Locate every Plasmodium falciparum-infected red blood cell.
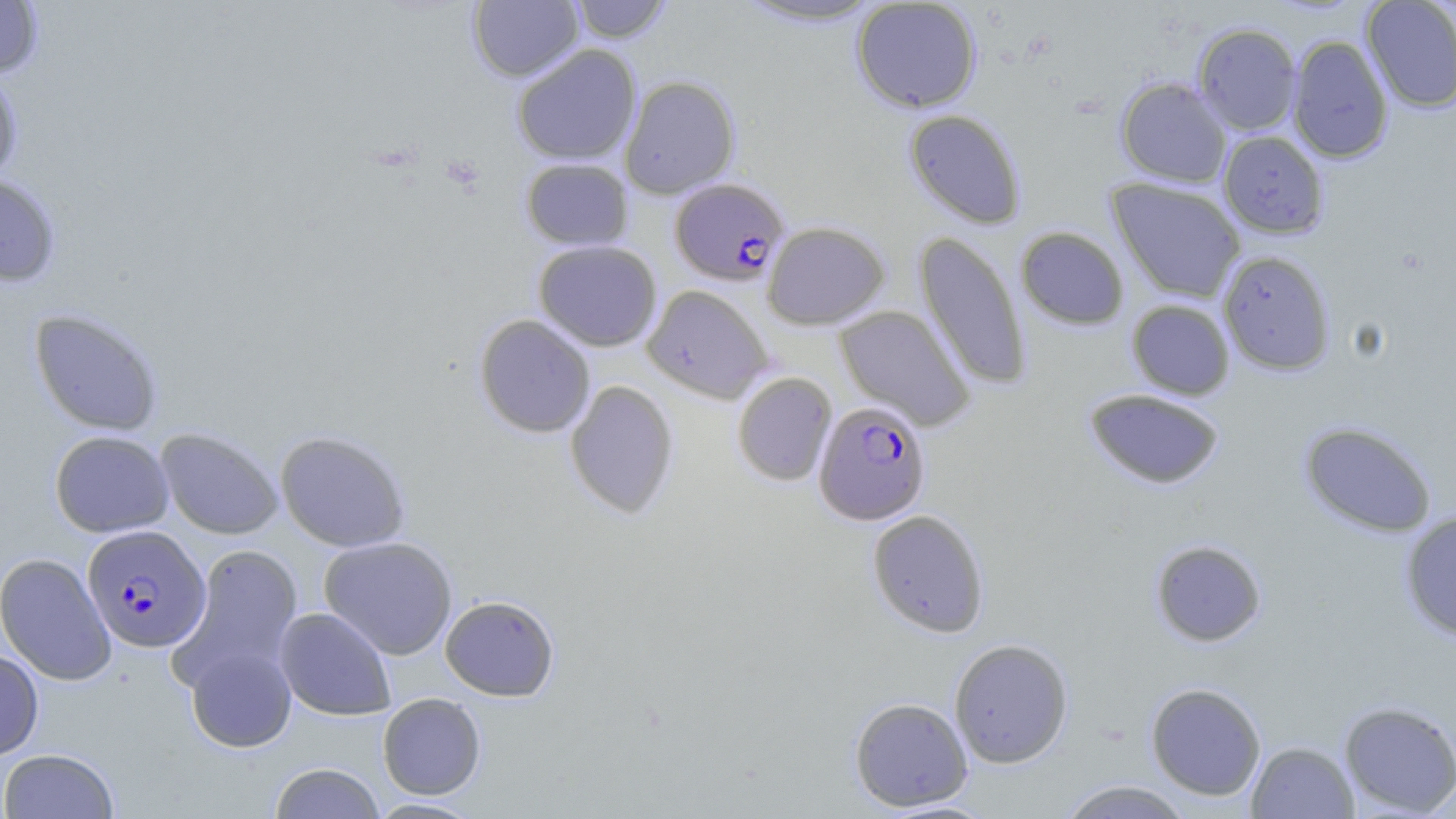
Approximate bounding boxes as (x1, y1, x2, y2) in pixels.
Plasmodium falciparum-infected red blood cells: (670, 178, 790, 286), (813, 400, 931, 525), (82, 525, 211, 653).

{
  "slide_level_diagnosis": "Plasmodium falciparum",
  "stain": "May-Grünwald-Giemsa",
  "image_size": "1456×819 pixels",
  "field_of_view": "single",
  "magnification": "1000x",
  "uninfected_red_blood_cell_locations": "approximate bounding boxes as (x1, y1, x2, y2) in pixels: (468, 0, 583, 82), (567, 0, 673, 43), (851, 0, 982, 113), (1361, 0, 1456, 113), (0, 1, 44, 79), (732, 1, 887, 28), (1193, 23, 1302, 135), (1287, 35, 1394, 163), (512, 44, 641, 165), (0, 67, 24, 186), (620, 75, 741, 199), (1116, 76, 1232, 188), (904, 109, 1027, 229), (1218, 131, 1329, 239), (520, 158, 634, 251), (0, 172, 61, 288), (1107, 178, 1246, 303), (762, 221, 889, 329), (1016, 226, 1129, 330), (914, 231, 1031, 391), (533, 240, 662, 351), (1218, 251, 1336, 376), (642, 285, 774, 404), (1127, 299, 1235, 400), (835, 305, 975, 431), (29, 308, 164, 435), (474, 314, 596, 438), (732, 372, 837, 487), (564, 380, 679, 519), (1083, 389, 1226, 490), (1299, 421, 1438, 538), (156, 427, 283, 540), (49, 430, 174, 537), (275, 430, 411, 552), (867, 509, 990, 637), (1399, 510, 1456, 641), (319, 536, 457, 660), (1149, 539, 1267, 647), (171, 544, 304, 690), (0, 552, 116, 686), (440, 595, 560, 701), (274, 607, 397, 720), (949, 638, 1074, 768), (185, 644, 297, 752), (0, 649, 44, 760), (1145, 682, 1266, 800), (377, 693, 486, 799), (849, 697, 973, 812), (1338, 700, 1456, 817), (1246, 741, 1359, 819), (0, 748, 120, 819), (269, 762, 384, 819), (1055, 779, 1196, 819), (365, 797, 484, 818), (875, 798, 1000, 818)",
  "modality": "optical microscopy",
  "preparation": "thin blood smear"
}